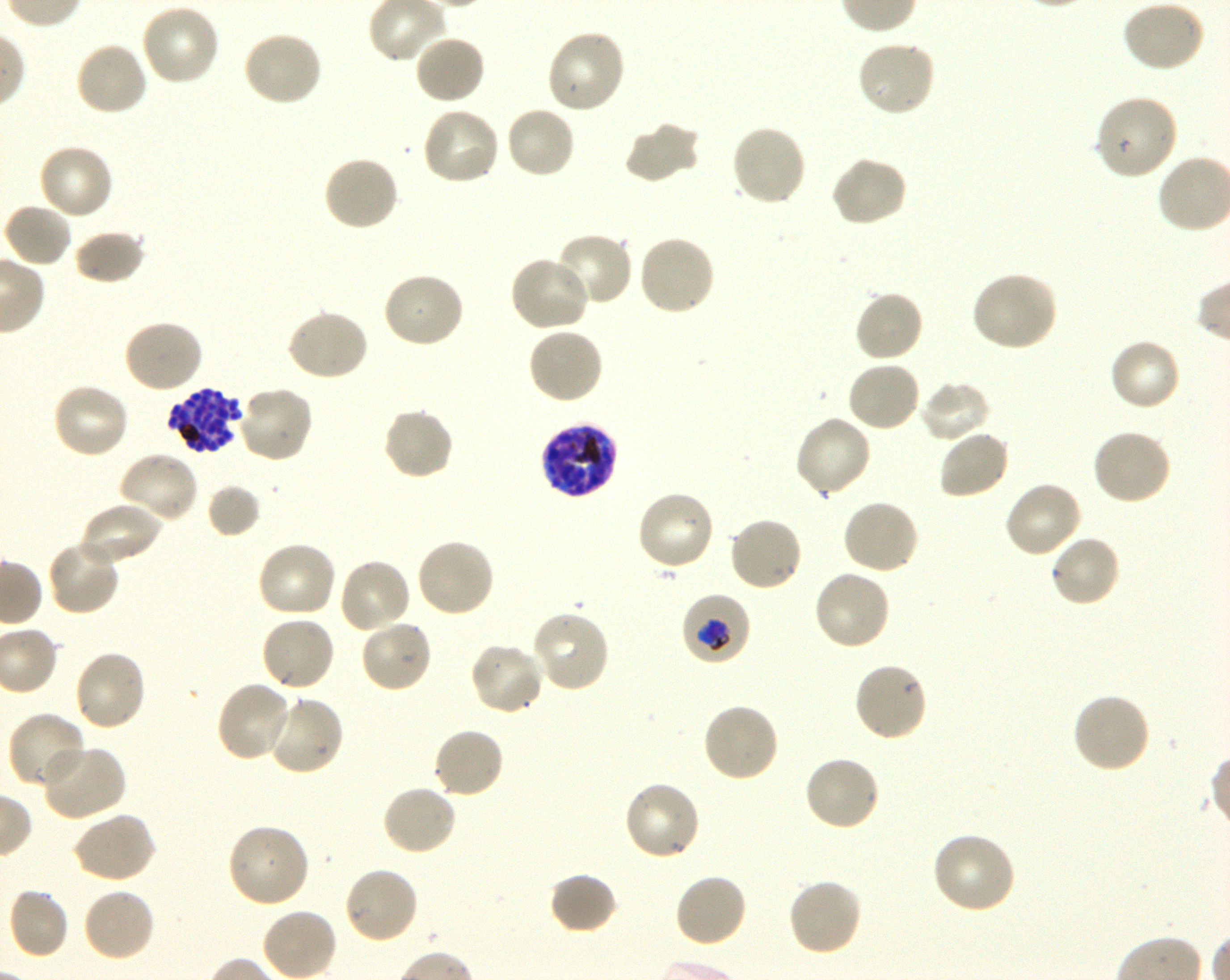

Approximate bounding rectangles given as corner coordinates in pixels from the top-left. Not every red blood cell is marked. A life-cycle stage — or a range of stages, where the recorded stages span more than one — follows each staged infected red blood cell.
Summary:
  - Locations of uninfected red blood cells: (x1=1120, y1=0, x2=1205, y2=72), (x1=140, y1=3, x2=222, y2=86), (x1=545, y1=29, x2=627, y2=116), (x1=241, y1=30, x2=323, y2=108), (x1=413, y1=34, x2=486, y2=106), (x1=856, y1=38, x2=937, y2=118), (x1=74, y1=41, x2=150, y2=118), (x1=1094, y1=93, x2=1180, y2=181), (x1=505, y1=104, x2=577, y2=179), (x1=421, y1=105, x2=501, y2=186), (x1=623, y1=122, x2=700, y2=184), (x1=730, y1=123, x2=808, y2=207), (x1=37, y1=143, x2=114, y2=221), (x1=322, y1=154, x2=400, y2=232), (x1=830, y1=154, x2=908, y2=228), (x1=2, y1=202, x2=73, y2=268), (x1=73, y1=230, x2=146, y2=286), (x1=552, y1=231, x2=633, y2=307), (x1=636, y1=235, x2=716, y2=317), (x1=508, y1=255, x2=593, y2=333), (x1=970, y1=269, x2=1058, y2=353), (x1=382, y1=271, x2=466, y2=349), (x1=853, y1=289, x2=924, y2=363), (x1=286, y1=308, x2=369, y2=383), (x1=122, y1=318, x2=203, y2=394), (x1=526, y1=326, x2=605, y2=405), (x1=1108, y1=338, x2=1181, y2=413), (x1=846, y1=359, x2=922, y2=433), (x1=918, y1=380, x2=992, y2=443), (x1=51, y1=382, x2=130, y2=461), (x1=236, y1=385, x2=314, y2=464), (x1=382, y1=406, x2=455, y2=481), (x1=793, y1=414, x2=873, y2=498), (x1=1092, y1=427, x2=1173, y2=507), (x1=937, y1=428, x2=1011, y2=500), (x1=116, y1=450, x2=200, y2=525), (x1=1003, y1=480, x2=1083, y2=559), (x1=636, y1=489, x2=716, y2=572), (x1=840, y1=498, x2=920, y2=575), (x1=78, y1=500, x2=163, y2=567), (x1=728, y1=515, x2=805, y2=592), (x1=1049, y1=534, x2=1121, y2=609), (x1=46, y1=537, x2=122, y2=616), (x1=415, y1=537, x2=496, y2=619), (x1=255, y1=541, x2=338, y2=620), (x1=337, y1=557, x2=413, y2=634), (x1=813, y1=570, x2=892, y2=652), (x1=530, y1=610, x2=612, y2=693), (x1=260, y1=615, x2=337, y2=692), (x1=359, y1=619, x2=434, y2=693), (x1=468, y1=640, x2=546, y2=716), (x1=72, y1=649, x2=148, y2=732), (x1=853, y1=660, x2=929, y2=742), (x1=215, y1=682, x2=296, y2=763), (x1=1071, y1=692, x2=1152, y2=774), (x1=266, y1=695, x2=345, y2=777), (x1=700, y1=701, x2=779, y2=784), (x1=7, y1=710, x2=88, y2=790), (x1=431, y1=726, x2=505, y2=800), (x1=40, y1=743, x2=127, y2=822), (x1=802, y1=754, x2=882, y2=832), (x1=623, y1=779, x2=703, y2=862), (x1=381, y1=783, x2=458, y2=856), (x1=72, y1=810, x2=156, y2=884), (x1=227, y1=823, x2=311, y2=908), (x1=931, y1=831, x2=1018, y2=915), (x1=342, y1=866, x2=419, y2=945), (x1=548, y1=872, x2=619, y2=936), (x1=674, y1=872, x2=749, y2=948), (x1=786, y1=876, x2=864, y2=957), (x1=8, y1=886, x2=69, y2=961), (x1=81, y1=887, x2=156, y2=963)
  - Locations of infected red blood cells: (x1=167, y1=387, x2=243, y2=456) late schizont; (x1=540, y1=420, x2=619, y2=498) schizont; (x1=680, y1=593, x2=751, y2=667) trophozoite
  - Life-cycle stages observed: trophozoite, schizont
  - Culture: Plasmodium falciparum strain 3D7, shaking, in vitro
  - Field of view: one from this slide
  - Stain: Giemsa
  - Image size: 1230×980 pixels
  - Preparation: thin blood film
  - Objective: 100x, oil immersion, numerical aperture 1.30
  - Donor blood group: O+